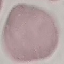

malaria status = uninfected
capture = smartphone through the microscope eyepiece
preparation = thin smear
image type = automatically extracted cell patch, resized to 64 × 64 pixels
stain = Giemsa